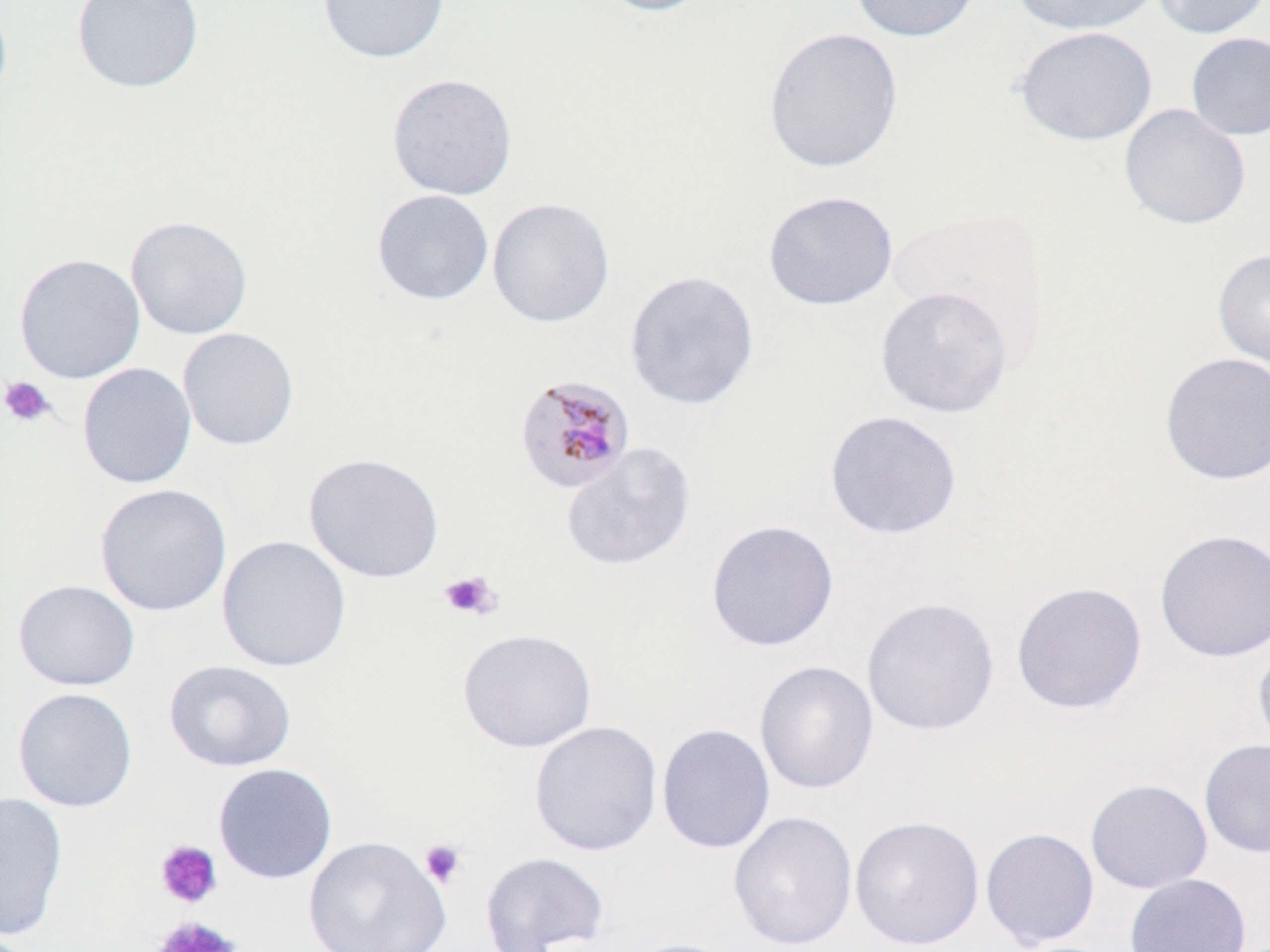
slide-level diagnosis = Plasmodium malariae
modality = optical microscopy
preparation = thin blood smear
image size = 1270×952 pixels
platelet locations = approximate bounding boxes as named x1/y1/x2/y2 corners in pixels: (x1=0, y1=376, x2=56, y2=427), (x1=439, y1=569, x2=502, y2=621), (x1=420, y1=839, x2=467, y2=889), (x1=155, y1=840, x2=222, y2=909), (x1=152, y1=915, x2=241, y2=952)
stain = May-Grünwald-Giemsa
uninfected red blood cell locations = approximate bounding boxes as named x1/y1/x2/y2 corners in pixels: (x1=0, y1=0, x2=13, y2=112), (x1=71, y1=0, x2=205, y2=94), (x1=317, y1=0, x2=450, y2=63), (x1=594, y1=0, x2=719, y2=17), (x1=848, y1=0, x2=981, y2=43), (x1=1011, y1=0, x2=1162, y2=36), (x1=1151, y1=0, x2=1270, y2=40), (x1=762, y1=26, x2=904, y2=173), (x1=1014, y1=26, x2=1158, y2=146), (x1=1185, y1=31, x2=1270, y2=141), (x1=386, y1=73, x2=518, y2=201), (x1=1119, y1=103, x2=1251, y2=231), (x1=371, y1=189, x2=494, y2=306), (x1=762, y1=190, x2=898, y2=312), (x1=487, y1=196, x2=615, y2=328), (x1=125, y1=215, x2=254, y2=341), (x1=1212, y1=247, x2=1270, y2=375), (x1=14, y1=253, x2=146, y2=384), (x1=624, y1=269, x2=760, y2=411), (x1=874, y1=285, x2=1014, y2=418), (x1=177, y1=327, x2=299, y2=452), (x1=1158, y1=352, x2=1270, y2=485), (x1=77, y1=362, x2=197, y2=490), (x1=824, y1=409, x2=962, y2=540), (x1=560, y1=442, x2=697, y2=571), (x1=303, y1=452, x2=445, y2=584), (x1=95, y1=483, x2=232, y2=616), (x1=705, y1=519, x2=839, y2=652), (x1=1154, y1=529, x2=1270, y2=663), (x1=216, y1=535, x2=352, y2=673), (x1=12, y1=580, x2=140, y2=691), (x1=1011, y1=581, x2=1147, y2=714), (x1=861, y1=596, x2=1000, y2=736), (x1=457, y1=628, x2=597, y2=753), (x1=1253, y1=641, x2=1270, y2=761), (x1=164, y1=659, x2=297, y2=773), (x1=754, y1=660, x2=879, y2=795), (x1=12, y1=687, x2=138, y2=812), (x1=529, y1=720, x2=663, y2=857), (x1=656, y1=723, x2=776, y2=855), (x1=1199, y1=739, x2=1270, y2=859), (x1=212, y1=763, x2=338, y2=884), (x1=1084, y1=779, x2=1213, y2=894), (x1=0, y1=792, x2=69, y2=942), (x1=727, y1=810, x2=858, y2=950), (x1=850, y1=815, x2=984, y2=950), (x1=979, y1=828, x2=1100, y2=950), (x1=303, y1=835, x2=452, y2=952), (x1=479, y1=850, x2=610, y2=952), (x1=1124, y1=873, x2=1252, y2=952), (x1=618, y1=937, x2=743, y2=952)
Plasmodium malariae-infected red blood cell locations = approximate bounding boxes as named x1/y1/x2/y2 corners in pixels: (x1=513, y1=375, x2=636, y2=495)
field of view = one of a larger specimen
magnification = 1000x